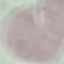

Summary:
  - Malaria status: uninfected
  - Image type: automatically extracted cell patch, resized to 64 × 64 pixels
  - Stain: Giemsa
  - Capture: smartphone through the microscope eyepiece
  - Preparation: thin blood film